Assess this cell for malaria.
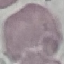

It is uninfected.

Summary:
  - Stain: Giemsa
  - Preparation: thin smear
  - Image type: automatically extracted cell patch, resized to 64 × 64 pixels
  - Capture: smartphone camera at the microscope eyepiece